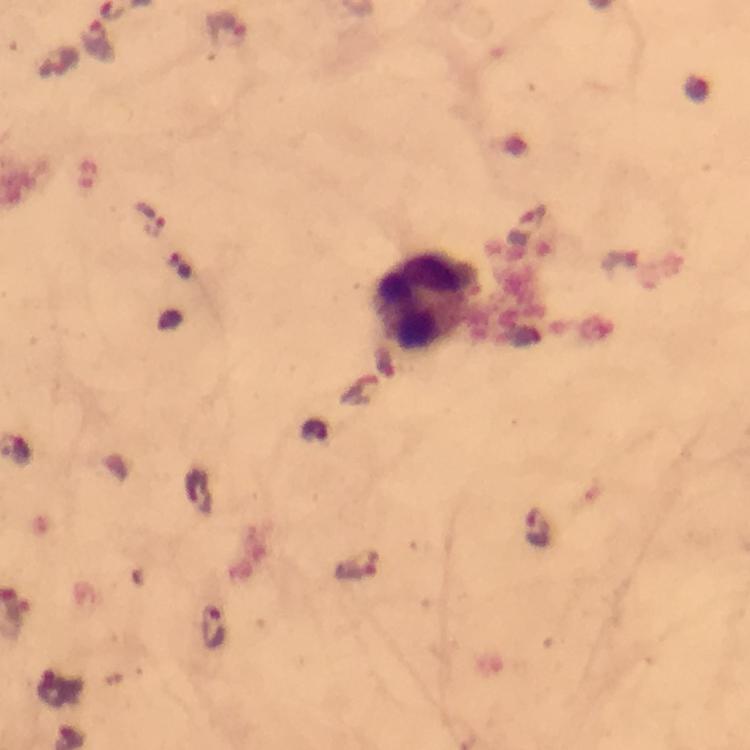
Approximate object centers, in pixels from the top-left corner. Malaria parasite locations: (x=226, y=29), (x=98, y=43), (x=148, y=218), (x=538, y=528), (x=359, y=567), (x=213, y=628). Leukocyte locations: (x=428, y=301). Thick blood smear. A crop from one field of view. Photographed through the microscope with a smartphone camera. At 100x magnification. From a malaria diagnostic workup. Giemsa-stained preparation. Image is 750×750 pixels. Immersion oil was used.